Classify this cell by malaria status.
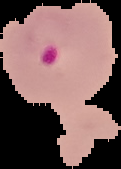

It is parasitized.

Summary:
  - Preparation: thin blood film
  - Image size: 121×169 pixels
  - Image type: segmented cell region on a black background